Describe the morphology of the erythrocytes.
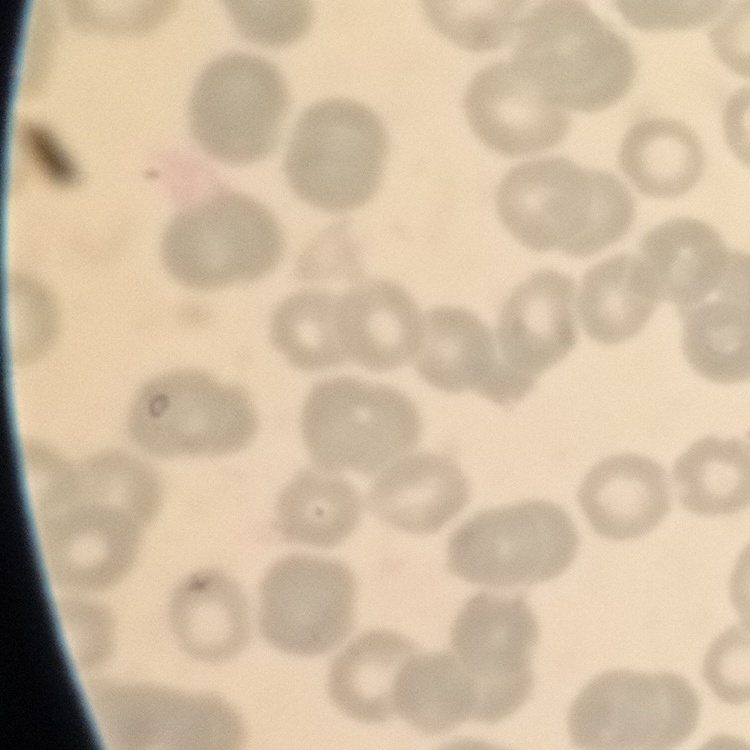

No rouleaux formation.

preparation = thin blood film
stain = Field's or Giemsa
image type = one tile cut from a larger photomicrograph